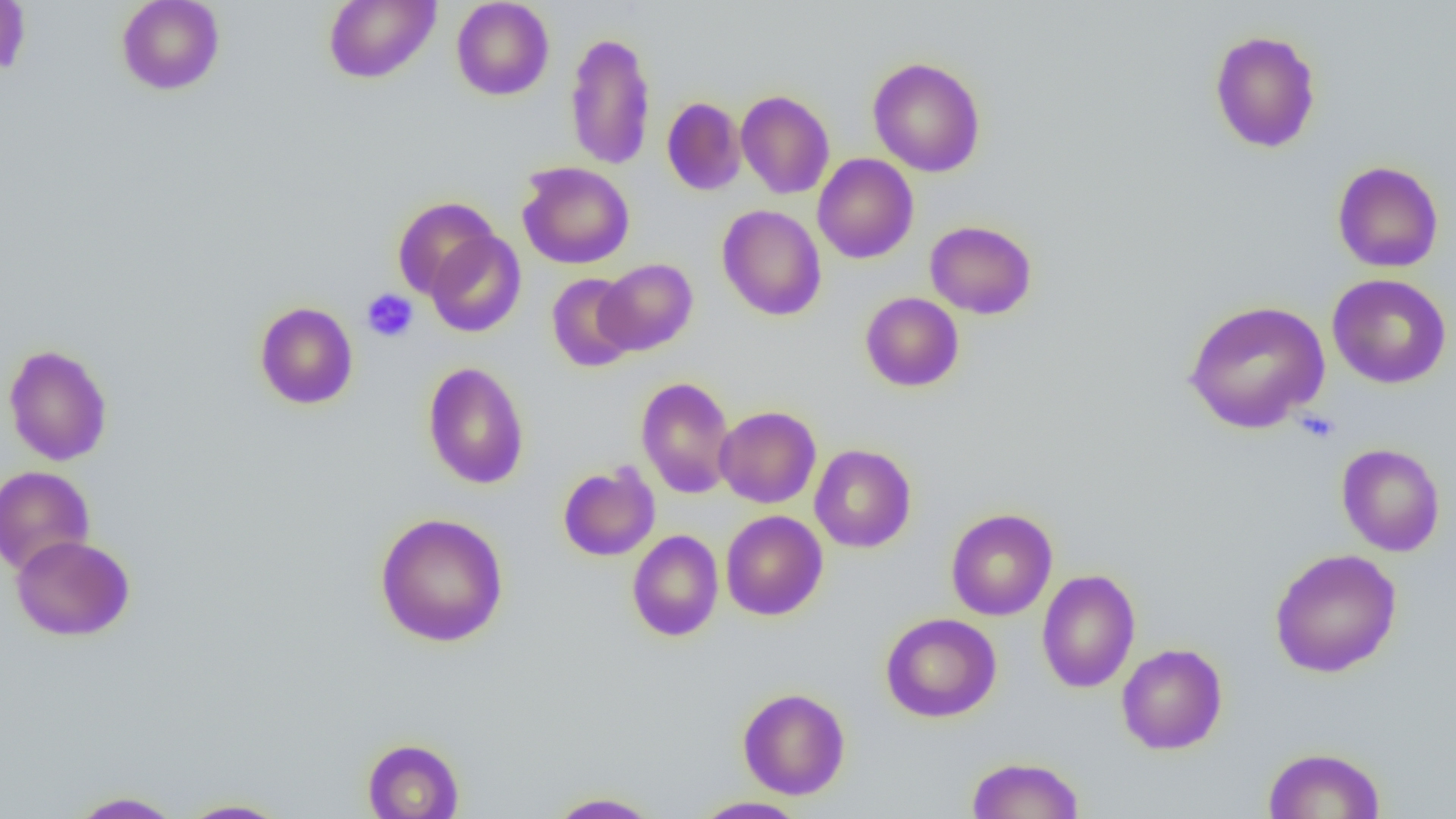

slide_level_diagnosis: negative for blood parasites
image_size: 1456×819 pixels
uninfected_red_blood_cell_locations: 'approximate bounding boxes as [x1, y1, x2, y2] in pixels: [0, 0, 31, 78], [116, 0, 225, 95], [323, 0, 440, 84], [451, 0, 554, 100], [565, 30, 656, 172], [1209, 30, 1322, 153], [868, 56, 986, 177], [735, 90, 835, 199], [661, 97, 746, 195], [813, 154, 918, 264], [1331, 160, 1444, 273], [517, 161, 634, 269], [392, 196, 501, 299], [717, 204, 827, 321], [925, 220, 1037, 319], [425, 230, 526, 338], [595, 259, 698, 355], [546, 273, 639, 372], [1327, 273, 1452, 389], [860, 292, 964, 392], [1183, 299, 1330, 433], [255, 301, 358, 410], [3, 344, 113, 466], [423, 361, 529, 490], [636, 376, 736, 499], [715, 405, 821, 508], [1336, 443, 1445, 556], [810, 444, 916, 553], [558, 463, 660, 561], [0, 465, 95, 576], [945, 508, 1058, 620], [720, 510, 828, 620], [374, 512, 509, 647], [627, 530, 724, 642], [11, 534, 135, 641], [1269, 548, 1402, 678], [1037, 569, 1140, 693], [880, 613, 1002, 722], [1116, 644, 1228, 755], [737, 687, 850, 799], [361, 738, 465, 818], [1262, 746, 1386, 818], [967, 756, 1085, 818], [68, 791, 184, 818], [546, 791, 662, 818], [691, 796, 810, 819], [177, 798, 292, 818]'
preparation: thin blood smear
magnification: 1000x
field_of_view: single
platelet_locations: 'approximate bounding boxes as [x1, y1, x2, y2] in pixels: [361, 289, 419, 342]'
modality: light microscopy